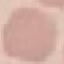

malaria_status: uninfected
image_type: cell patch, automatically extracted from a larger field of view and resized to 64 × 64 pixels
capture: smartphone through the microscope eyepiece
stain: Giemsa
preparation: thin smear